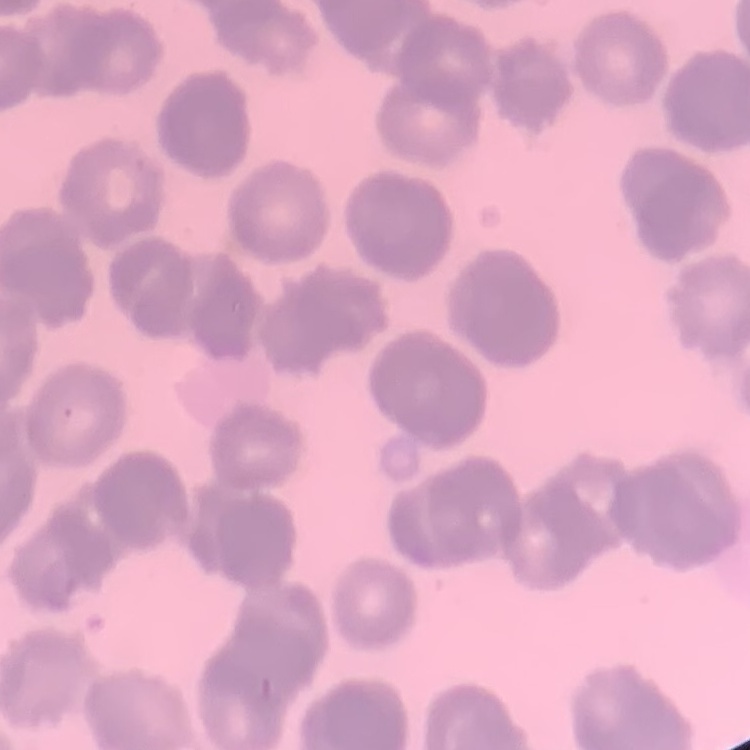

Summary:
  - Erythrocyte morphology: rouleaux formation
  - Preparation: thin peripheral smear
  - Stain: Field's or Giemsa
  - Image type: square crop of a larger photomicrograph